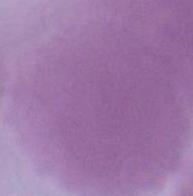
{
  "magnification": "1000x",
  "identification": "erythrocyte",
  "modality": "micrograph"
}